Comment on the morphology of the red blood cells.
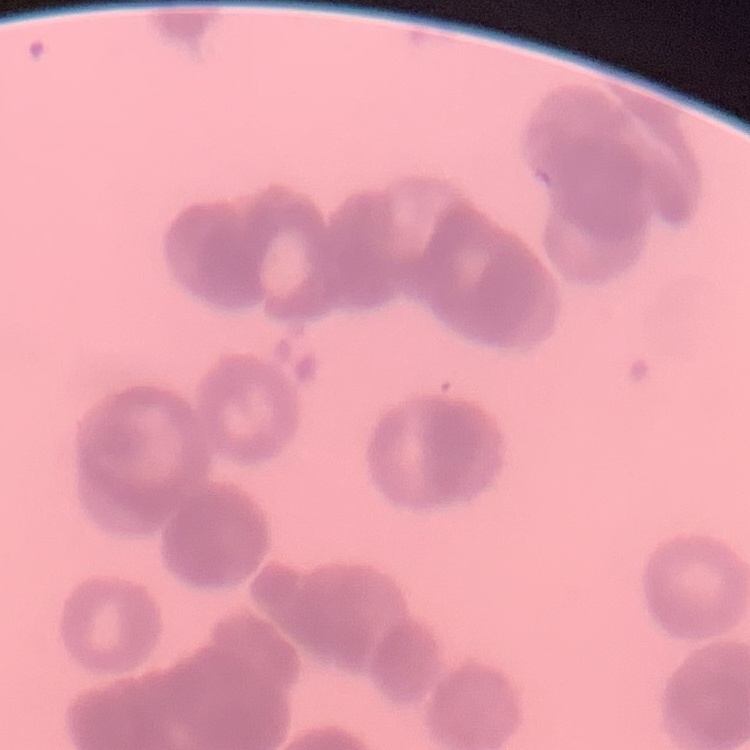
Rouleaux formation.

Thin blood film. Stained with either Field's or Giemsa. Square crop of a larger photomicrograph.